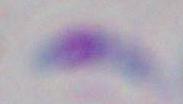

Summary:
  - Modality: micrograph
  - Identification: Toxoplasma gondii
  - Magnification: 1000x